Name the parasite shown.
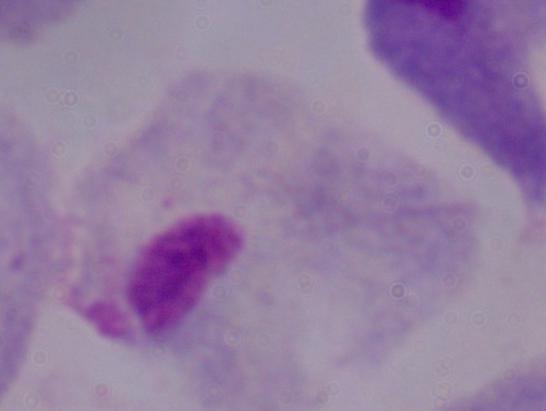
This is a trichomonad.

magnification = 1000x
modality = micrograph